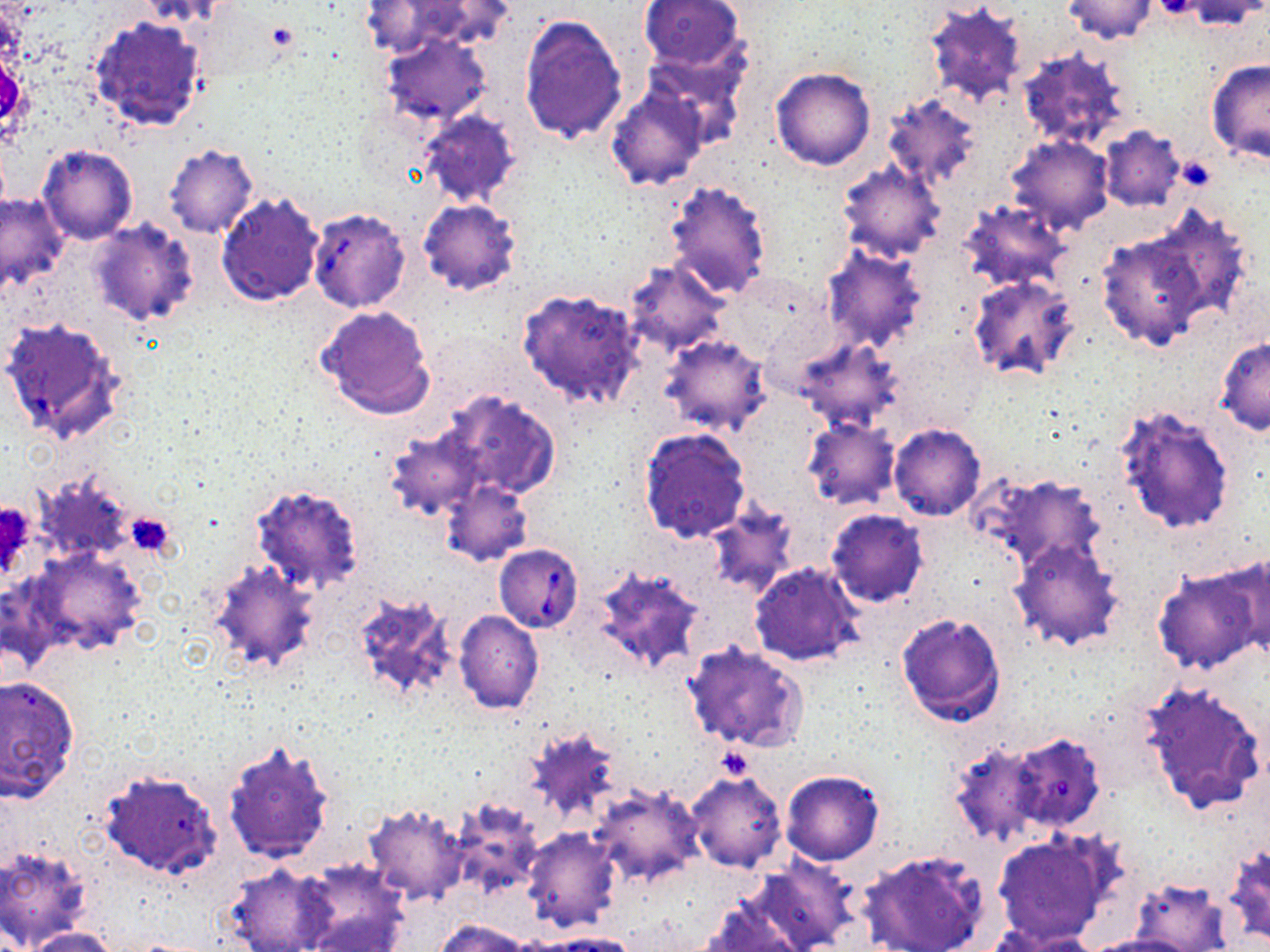

Summary:
  - Coordinate format: approximate bounding boxes as (x1, y1, x2, y2) in pixels
  - Babesia divergens-infected red blood cell locations: (307, 208, 412, 313), (494, 544, 583, 632)
  - Platelet locations: (1154, 0, 1201, 20), (266, 22, 297, 51), (126, 512, 176, 557), (716, 746, 753, 783)
  - Uninfected red blood cell locations: (1061, 0, 1157, 44), (1178, 0, 1266, 30), (138, 1, 239, 29), (639, 1, 746, 72), (925, 2, 1026, 109), (518, 14, 628, 146), (90, 15, 209, 136), (381, 33, 490, 124), (1016, 48, 1133, 153), (1205, 58, 1270, 165), (771, 68, 874, 171), (607, 87, 708, 191), (883, 91, 982, 188), (417, 110, 521, 210), (1097, 126, 1187, 213), (1006, 136, 1112, 234), (164, 144, 259, 239), (37, 145, 138, 245), (836, 159, 945, 262), (662, 179, 773, 300), (217, 191, 325, 306), (0, 192, 70, 292), (417, 199, 522, 296), (956, 199, 1070, 294), (1143, 204, 1255, 321), (88, 220, 199, 328), (1095, 226, 1212, 353), (821, 244, 929, 354), (622, 260, 728, 355), (967, 275, 1082, 384), (517, 288, 645, 409), (318, 305, 437, 419), (660, 335, 772, 438), (1214, 336, 1270, 435), (796, 337, 905, 434), (441, 389, 563, 500), (1113, 402, 1239, 535), (803, 419, 900, 511), (888, 424, 987, 521), (385, 427, 484, 520), (637, 427, 751, 543), (32, 468, 138, 566), (970, 470, 1108, 574), (440, 479, 533, 566), (250, 484, 365, 596), (704, 502, 798, 598), (826, 509, 928, 607), (1009, 536, 1126, 649), (25, 547, 148, 659), (1219, 552, 1270, 658), (205, 560, 321, 675), (749, 561, 865, 668), (590, 565, 706, 676), (1154, 568, 1262, 675), (349, 589, 460, 707), (453, 610, 544, 715), (896, 612, 1007, 727), (683, 641, 809, 754), (0, 674, 79, 803), (1139, 679, 1267, 817), (521, 721, 628, 828), (1005, 732, 1107, 834), (222, 740, 335, 865), (948, 741, 1046, 847), (101, 769, 221, 879), (780, 769, 885, 866), (687, 771, 788, 872), (589, 783, 705, 888), (445, 795, 546, 903), (361, 803, 470, 907), (521, 828, 622, 932), (992, 830, 1115, 946), (1223, 844, 1270, 947), (0, 845, 93, 948), (857, 848, 989, 952), (749, 855, 857, 952), (293, 861, 408, 952), (222, 863, 333, 952), (1131, 877, 1232, 952), (697, 899, 805, 952), (435, 918, 530, 952), (21, 926, 121, 952), (1003, 930, 1104, 952), (545, 932, 641, 952), (1079, 935, 1192, 952)
  - Slide-level diagnosis: Babesia divergens
  - Preparation: thin blood film
  - Stain: May-Grünwald-Giemsa
  - Image size: 1270×952 pixels
  - Field of view: one of a larger specimen
  - Modality: light microscopy
  - Magnification: 1000x